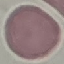

Summary:
  - Result: no malaria parasites detected
  - Stain: Giemsa
  - Image type: automatically extracted cell patch, resized to 64 × 64 pixels
  - Capture: smartphone camera at the microscope eyepiece
  - Preparation: thin blood film